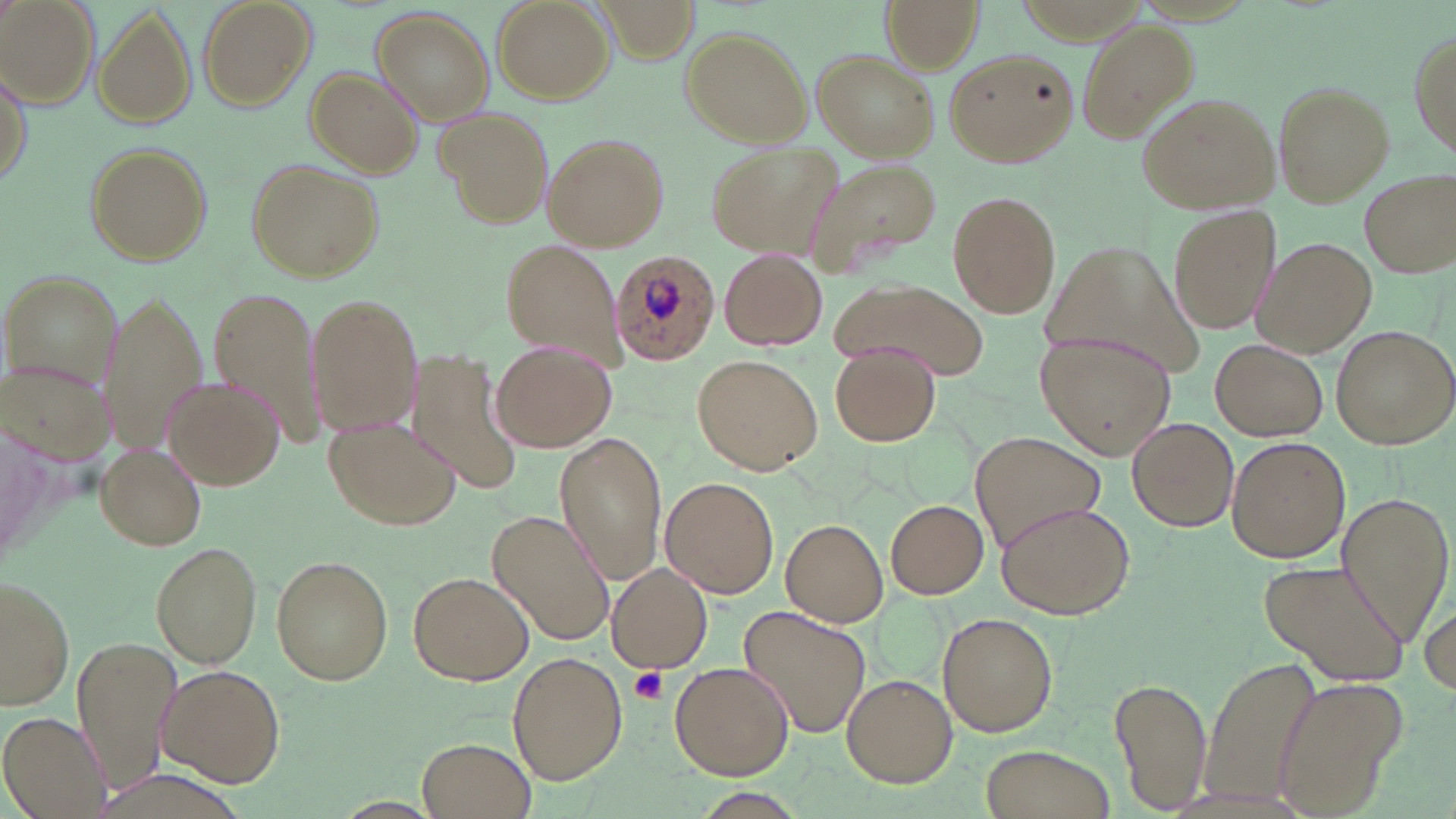
Approximate bounding boxes as (x1, y1, x2, y2) in pixels. Platelet locations: (629, 666, 668, 705). Plasmodium ovale-infected red blood cell locations: (609, 249, 723, 363). Uninfected red blood cell locations: (197, 0, 315, 109), (493, 0, 614, 103), (1, 1, 98, 107), (881, 1, 983, 71), (94, 6, 199, 130), (372, 8, 494, 124), (1079, 19, 1195, 141), (1409, 25, 1456, 164), (678, 27, 813, 149), (944, 48, 1079, 168), (814, 50, 938, 162), (1, 62, 32, 193), (304, 67, 423, 178), (1273, 81, 1395, 207), (1139, 93, 1280, 213), (435, 103, 548, 225), (543, 134, 669, 251), (83, 140, 213, 265), (706, 141, 843, 257), (249, 158, 383, 280), (806, 158, 943, 279), (1362, 171, 1455, 276), (947, 189, 1061, 318), (1167, 203, 1283, 335), (1255, 236, 1377, 357), (501, 237, 626, 370), (1037, 243, 1207, 381), (719, 247, 827, 351), (6, 270, 125, 393), (844, 279, 989, 382), (102, 291, 206, 452), (208, 291, 322, 441), (307, 293, 423, 438), (1330, 325, 1454, 449), (1035, 330, 1176, 459), (1211, 339, 1328, 440), (493, 342, 616, 452), (830, 346, 940, 447), (407, 353, 523, 496), (693, 354, 822, 475), (163, 376, 284, 489), (323, 414, 463, 530), (1126, 415, 1238, 532), (555, 432, 667, 583), (971, 433, 1106, 550), (1226, 438, 1349, 563), (95, 444, 207, 550), (660, 476, 777, 599), (1334, 488, 1455, 647), (994, 497, 1135, 619), (885, 499, 988, 599), (486, 510, 617, 647), (782, 519, 889, 625), (150, 542, 262, 667), (271, 555, 393, 686), (1260, 558, 1409, 686), (607, 563, 713, 673), (408, 570, 535, 685), (0, 573, 74, 714), (1419, 586, 1455, 704), (735, 606, 873, 738), (939, 614, 1057, 735), (72, 633, 184, 795), (507, 651, 628, 784), (1199, 652, 1318, 809), (669, 662, 793, 779), (155, 663, 286, 787), (1112, 671, 1209, 814), (840, 674, 957, 790), (1269, 679, 1403, 819), (1, 709, 110, 817), (417, 737, 535, 819), (977, 742, 1117, 819). Slide-level diagnosis: Plasmodium ovale. May-Grünwald-Giemsa stain. One field of a larger specimen. Captured at 1000x magnification. Image is 1456×819 pixels. Thin blood film. Optical microscopy.